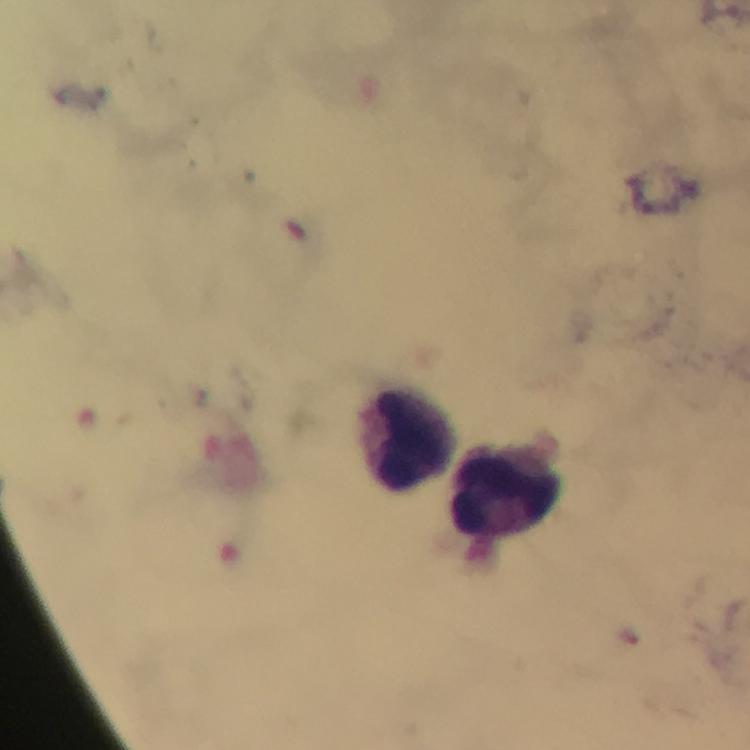

Approximate object centers, in pixels from the top-left corner.
Summary:
  - Leukocyte locations: (x=406, y=438), (x=509, y=494)
  - Capture: smartphone camera through the microscope
  - Magnification: 100x
  - Preparation: thick blood smear
  - Stain: Giemsa
  - Image size: 750×750 pixels
  - Malaria parasites: none seen
  - Cropped from: a single field of view
  - Immersion oil: applied
  - Context: from a diagnostic examination for malaria